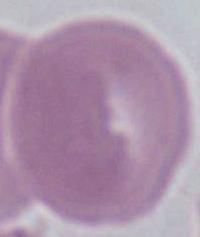

Summary:
  - Identification: erythrocyte
  - Modality: micrograph
  - Magnification: 1000x